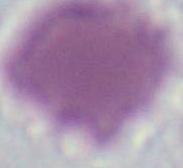
An erythrocyte is shown. Captured at 1000x magnification. Photomicrograph.